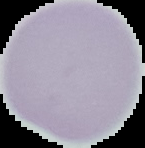

image_type: cell region segmented out of the field of view; surrounding area masked to black
preparation: thin blood film
image_size: 145×148 pixels
malaria_status: uninfected